Locate and identify every blood parasite.
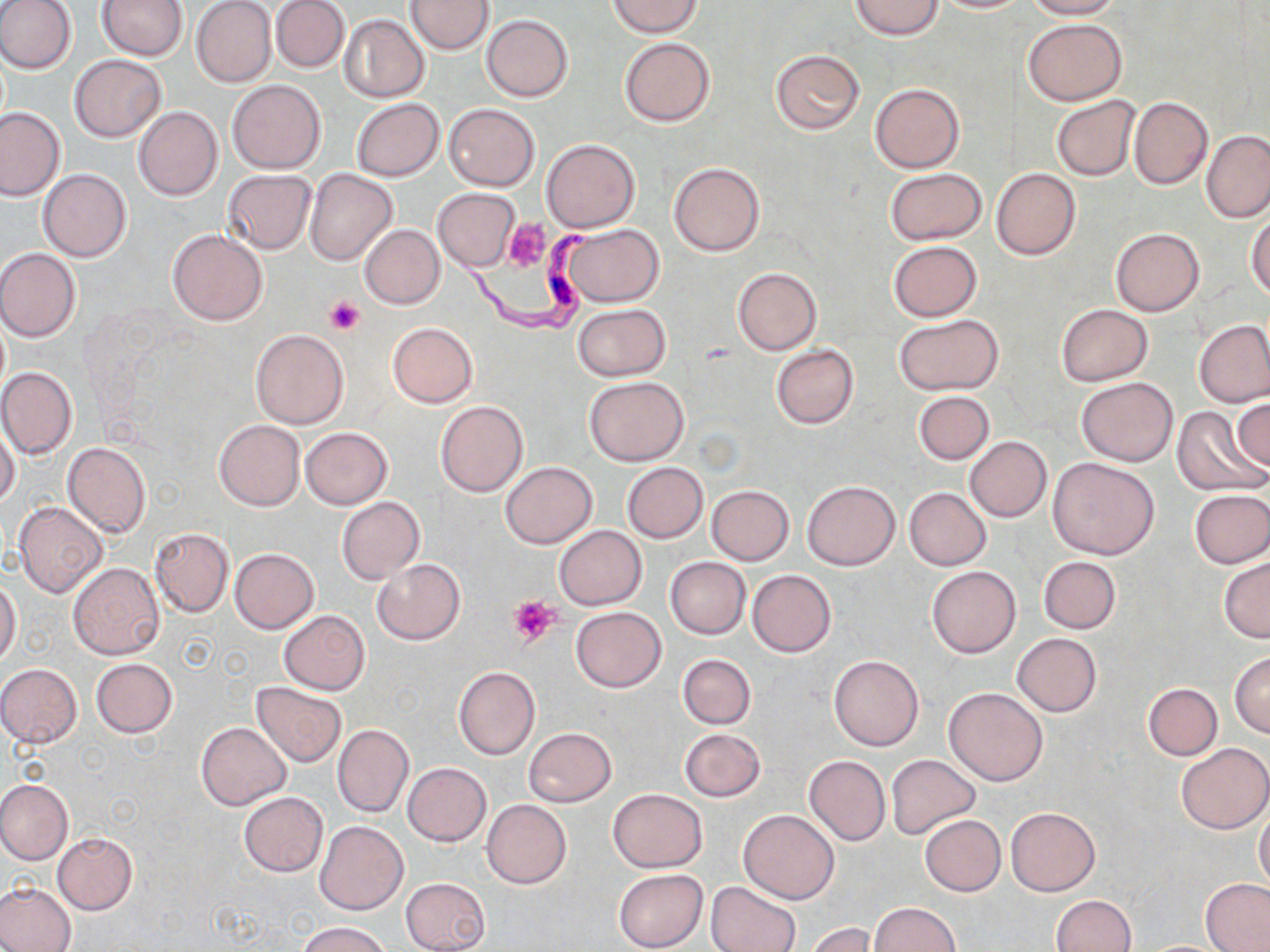

Approximate bounding boxes as (x1, y1, x2, y2) in pixels.
Trypanosoma brucei: (445, 208, 595, 333).
No Plasmodium falciparum, Plasmodium ovale, Plasmodium malariae, Plasmodium vivax, or Babesia divergens observed.

Summary:
  - Platelet locations: (503, 219, 552, 273), (325, 294, 365, 334), (508, 596, 561, 648)
  - Uninfected red blood cell locations: (0, 0, 75, 74), (97, 0, 187, 61), (271, 0, 349, 73), (849, 0, 943, 39), (930, 0, 1029, 13), (1023, 0, 1123, 19), (191, 1, 276, 88), (404, 1, 494, 53), (608, 1, 702, 37), (340, 14, 430, 103), (481, 14, 573, 102), (1023, 18, 1126, 104), (619, 37, 715, 126), (770, 49, 865, 134), (70, 55, 167, 142), (227, 80, 325, 173), (870, 83, 965, 172), (1051, 96, 1140, 182), (1129, 97, 1212, 189), (351, 98, 444, 181), (443, 103, 540, 191), (0, 106, 67, 201), (134, 106, 223, 201), (1202, 129, 1270, 224), (542, 139, 640, 232), (670, 162, 764, 257), (885, 168, 986, 245), (992, 168, 1080, 260), (38, 169, 131, 262), (220, 169, 316, 254), (305, 169, 399, 266), (433, 187, 521, 272), (1248, 212, 1270, 300), (558, 223, 665, 307), (359, 225, 445, 309), (1111, 228, 1204, 316), (167, 229, 268, 326), (887, 240, 981, 322), (0, 248, 81, 342), (733, 267, 822, 356), (573, 304, 670, 381), (1056, 304, 1153, 386), (894, 314, 1004, 396), (1194, 319, 1270, 407), (388, 321, 478, 407), (249, 330, 347, 428), (770, 344, 858, 429), (0, 366, 77, 461), (584, 376, 689, 466), (1076, 377, 1178, 467), (913, 390, 994, 465), (1233, 396, 1270, 475), (435, 399, 528, 497), (1172, 407, 1265, 497), (214, 420, 305, 511), (0, 424, 20, 508), (300, 427, 392, 509), (964, 436, 1052, 523), (62, 442, 151, 538), (1048, 457, 1160, 560), (500, 462, 597, 547), (622, 462, 708, 543), (803, 480, 900, 569), (707, 484, 794, 564), (905, 487, 991, 570), (1189, 488, 1270, 568), (336, 497, 424, 582), (15, 502, 106, 598), (553, 525, 647, 610), (149, 528, 233, 617), (229, 548, 318, 634), (1038, 556, 1122, 634), (372, 558, 465, 644), (665, 558, 749, 639), (1219, 558, 1270, 642), (69, 562, 164, 659), (927, 566, 1020, 657), (747, 570, 836, 657), (0, 578, 21, 665), (571, 606, 666, 692), (278, 610, 370, 694), (1012, 632, 1102, 716), (1230, 651, 1270, 737), (677, 654, 757, 729), (829, 654, 923, 751), (91, 658, 177, 737), (0, 663, 83, 748), (453, 666, 540, 759), (251, 681, 348, 767), (1142, 682, 1223, 760), (945, 686, 1046, 785), (196, 722, 291, 809), (333, 724, 414, 816), (524, 727, 617, 806), (678, 728, 766, 802), (1176, 743, 1269, 834), (886, 754, 979, 840), (804, 756, 890, 845), (403, 763, 491, 847), (0, 780, 72, 864), (608, 788, 708, 872), (238, 793, 328, 878), (481, 799, 571, 888), (1254, 804, 1270, 890), (1005, 807, 1100, 896), (738, 810, 839, 904), (920, 815, 1005, 896), (315, 820, 407, 915), (53, 832, 138, 913), (614, 868, 708, 951), (401, 877, 491, 952), (1201, 878, 1270, 951), (707, 881, 799, 952), (0, 882, 75, 952), (1050, 895, 1135, 952), (869, 903, 961, 952), (298, 921, 393, 952), (807, 923, 877, 952)
  - Slide-level diagnosis: Trypanosoma brucei
  - Stain: May-Grünwald-Giemsa
  - Image size: 1270×952 pixels
  - Preparation: thin blood film
  - Magnification: 1000x
  - Modality: optical microscopy
  - Field of view: one of a larger specimen